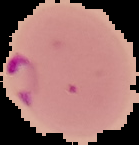
Image is 139×145 pixels. Malaria status: parasitized. Cell region segmented out of the field of view; the surrounding area is masked to black. From a thin blood smear.